Report the malaria status of this cell.
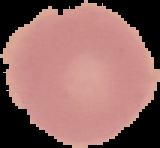
Uninfected.

Summary:
  - Preparation: thin blood smear
  - Image size: 160×148 pixels
  - Image type: segmented cell region with the area outside set to black